Comment on the morphology of the red blood cells.
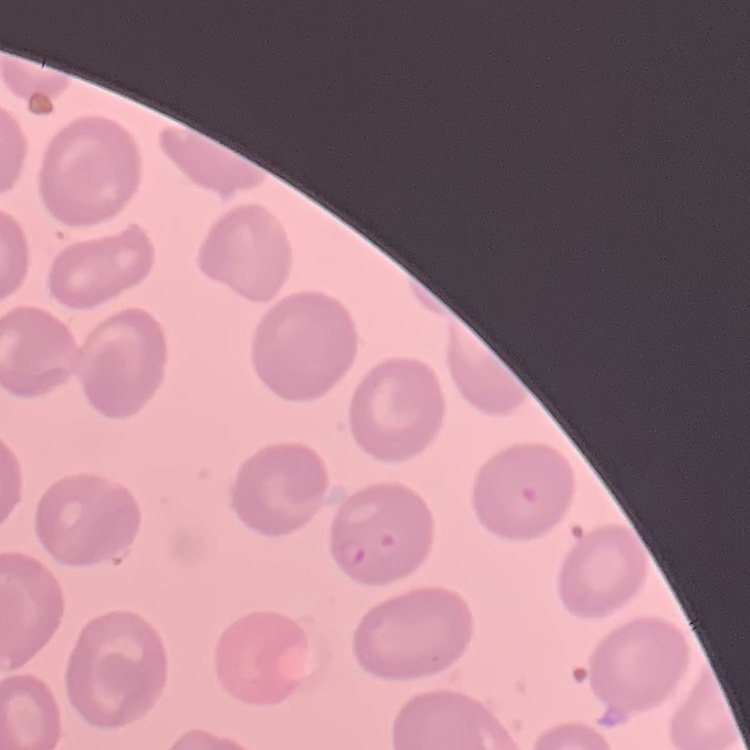
No rouleaux formation.

Square crop of a larger photomicrograph. Field's or Giemsa stain. Thin peripheral smear.